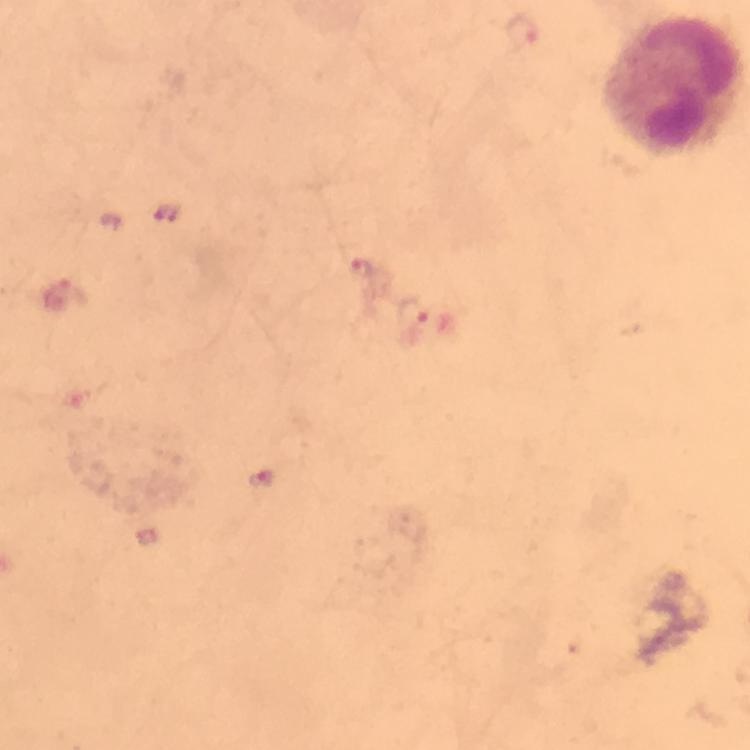
immersion_oil: applied
preparation: thick blood film
context: from a diagnostic examination for malaria
capture: smartphone mounted on the microscope
magnification: 100x
stain: Giemsa
plasmodium_parasite_locations: 'approximate centers as {x, y} in pixels: {524, 32}, {167, 213}, {360, 268}, {412, 311}, {261, 480}'
image_size: 750×750 pixels
cropped_from: a single field of view